Outline platelets.
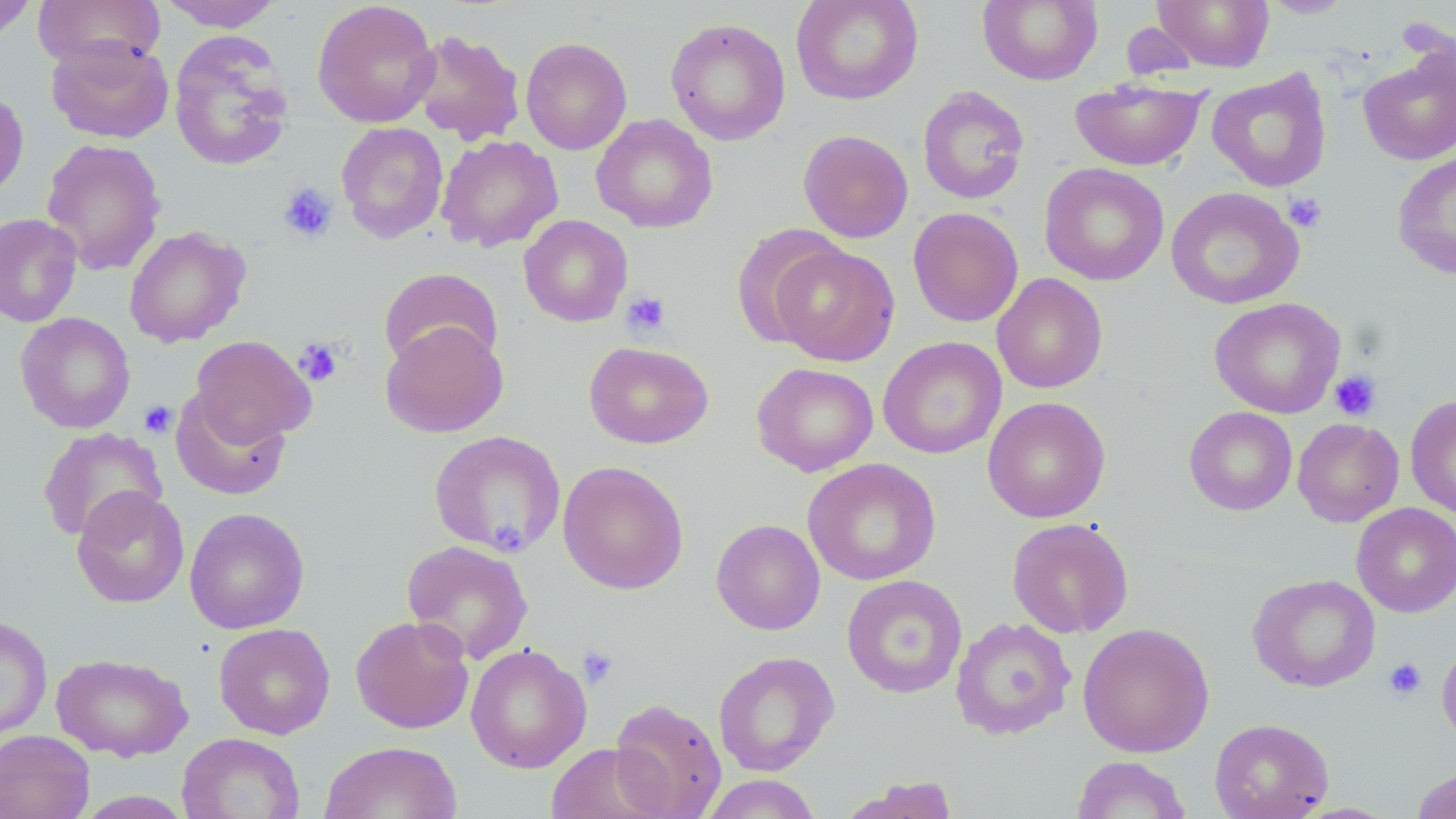

Approximate bounding boxes as (x1,y1)-(x2,y2) corner pairs in pixels.
Platelets: (278,182)-(339,243), (1284,192)-(1327,232), (621,290)-(672,338), (293,337)-(343,387), (1329,370)-(1382,421), (139,401)-(177,438), (577,646)-(619,689), (1383,657)-(1427,701).

Uninfected red blood cell locations: (157,0)-(283,31), (791,0)-(923,105), (977,0)-(1103,86), (1152,0)-(1274,71), (1259,0)-(1355,18), (0,1)-(37,43), (34,1)-(165,72), (312,1)-(440,128), (664,17)-(791,146), (409,29)-(525,146), (168,31)-(295,171), (47,35)-(174,144), (520,37)-(632,155), (1358,47)-(1456,166), (1206,67)-(1332,193), (1070,74)-(1333,180), (1070,78)-(1206,171), (917,86)-(1030,205), (0,88)-(29,202), (591,114)-(718,233), (336,123)-(448,243), (798,129)-(913,243), (436,135)-(563,252), (41,138)-(167,276), (1392,150)-(1456,279), (1039,163)-(1169,286), (1166,186)-(1305,310), (908,207)-(1023,327), (0,213)-(82,327), (518,214)-(633,327), (731,223)-(845,347), (124,225)-(250,348), (769,243)-(901,366), (378,266)-(503,371), (992,273)-(1108,393), (1209,297)-(1345,418), (16,312)-(135,433), (380,321)-(508,438), (190,335)-(315,446), (878,337)-(1006,459), (584,341)-(714,449), (752,362)-(879,477), (170,391)-(291,501), (1405,395)-(1456,520), (982,396)-(1111,523), (1184,406)-(1297,515), (1292,417)-(1404,527), (37,427)-(168,543), (428,430)-(566,557), (803,458)-(941,586), (557,460)-(689,595), (71,486)-(190,608), (1351,503)-(1456,617), (184,507)-(310,634), (1006,517)-(1134,638), (711,518)-(825,635), (401,540)-(534,664), (1247,573)-(1381,692), (841,574)-(967,698), (0,615)-(52,740), (350,615)-(475,734), (950,616)-(1077,740), (1077,621)-(1215,758), (214,623)-(335,739), (1436,637)-(1456,746), (465,643)-(592,773), (713,650)-(840,776), (51,652)-(193,762), (609,697)-(727,818), (1209,717)-(1334,819), (0,729)-(95,819), (177,731)-(305,819), (320,740)-(462,819), (544,742)-(669,819), (1071,755)-(1193,818), (1410,767)-(1456,819), (698,774)-(824,818), (839,776)-(961,819), (72,790)-(195,818). Slide-level diagnosis: negative for blood parasites. One field of a larger specimen. May-Grünwald-Giemsa stain. 1000x magnification. Image is 1456×819 pixels. Thin blood film. Light microscopy.